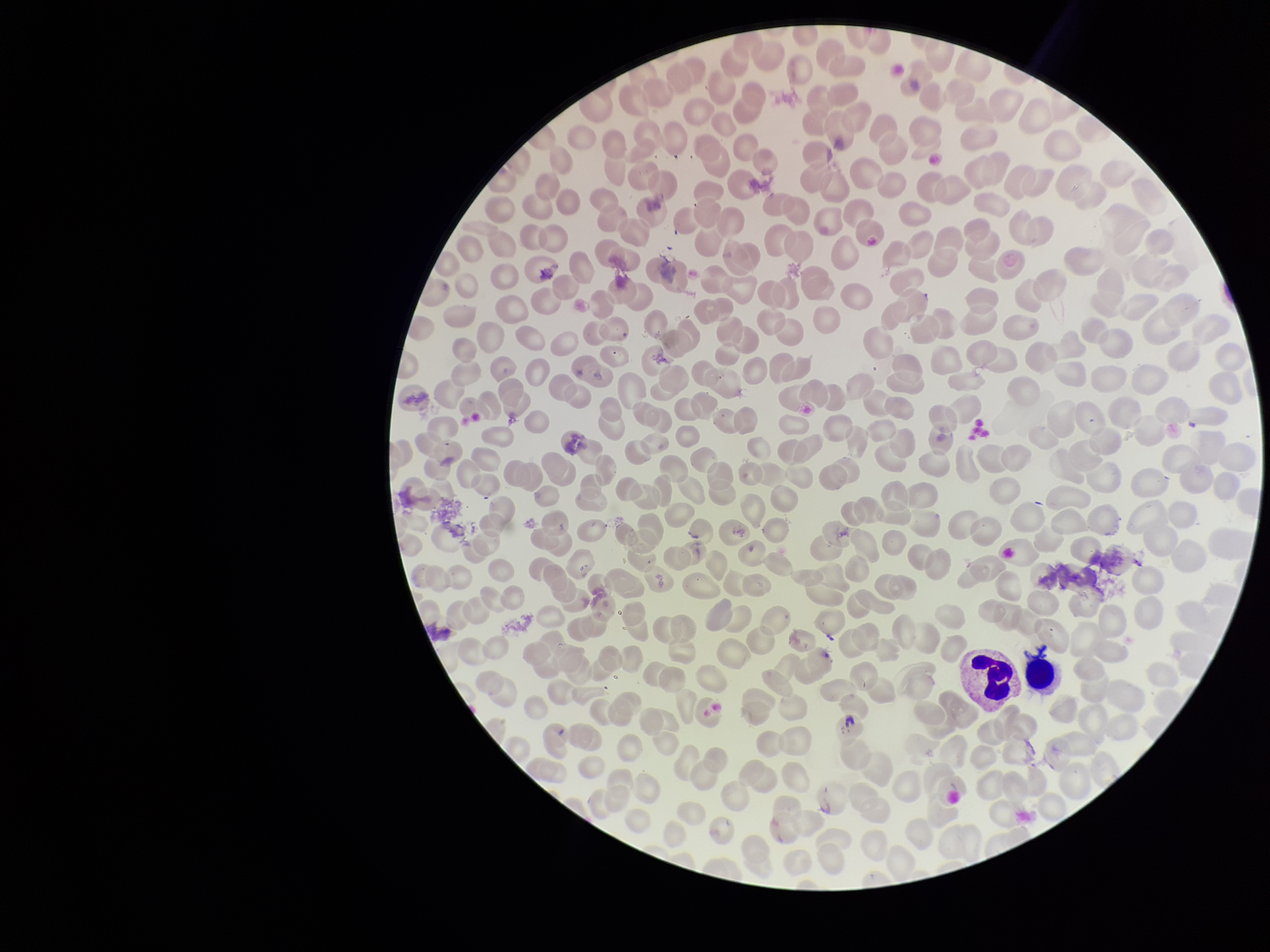

Red blood cell count: 225. Smartphone photograph taken through the eyepiece of a microscope. Preparation: thin smear. Parasitized red blood cells: none detected. Parasitized red blood cell count: 0. Image is 1270×952 pixels. Giemsa stain. Patient malaria status: negative. One field from this slide.